Locate every Plasmodium falciparum-infected red blood cell.
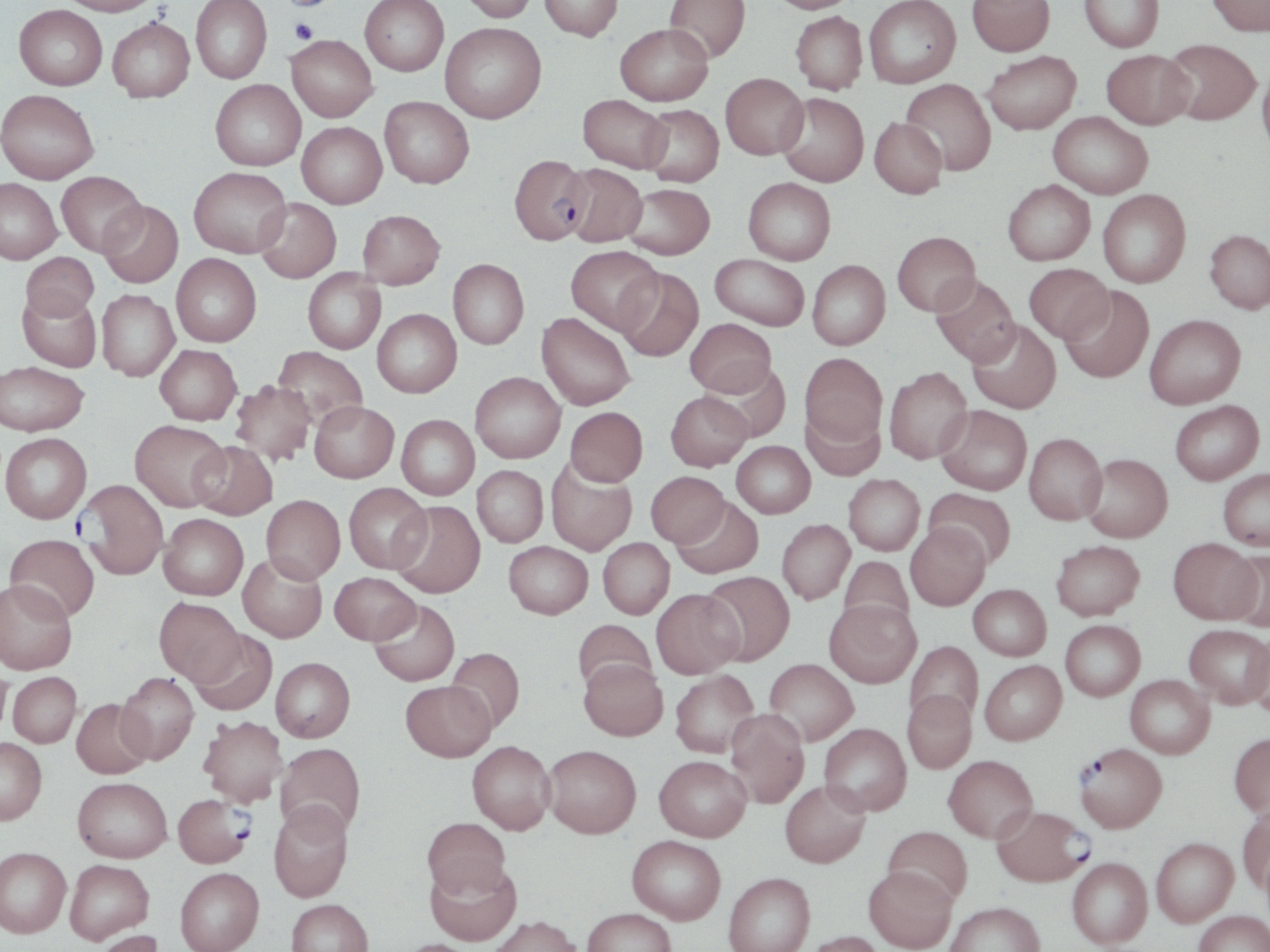

Approximate bounding boxes as (x1,y1)-(x2,y2) corner pairs in pixels.
Plasmodium falciparum-infected red blood cells: (509,154)-(591,244), (77,479)-(168,580), (1075,743)-(1168,832), (173,793)-(253,867), (992,805)-(1091,887).

slide-level diagnosis = Plasmodium falciparum
stain = May-Grünwald-Giemsa
uninfected red blood cell locations = approximate bounding boxes as (x1,y1)-(x2,y2) corner pairs in pixels: (59,0)-(161,16), (191,0)-(272,83), (360,0)-(448,76), (458,0)-(539,22), (540,0)-(623,41), (664,0)-(751,62), (767,0)-(863,13), (863,0)-(961,88), (967,0)-(1054,55), (1079,0)-(1164,52), (1207,0)-(1270,36), (14,4)-(107,90), (790,11)-(868,94), (108,18)-(194,102), (440,22)-(546,123), (615,23)-(712,105), (286,35)-(377,121), (1162,38)-(1261,125), (1101,49)-(1194,129), (982,50)-(1081,134), (1257,64)-(1270,161), (720,73)-(808,159), (210,79)-(306,171), (901,79)-(996,175), (0,89)-(99,183), (777,93)-(869,187), (578,94)-(671,173), (379,96)-(474,188), (639,105)-(724,187), (1048,111)-(1152,199), (869,117)-(947,199), (297,122)-(386,208), (562,163)-(647,247), (189,167)-(291,257), (56,171)-(146,256), (0,177)-(62,264), (743,177)-(835,265), (1003,179)-(1095,265), (622,183)-(715,259), (1097,189)-(1191,287), (254,198)-(341,283), (98,200)-(183,287), (358,209)-(445,288), (1205,229)-(1270,314), (892,231)-(980,316), (566,245)-(662,334), (21,252)-(99,321), (172,253)-(261,347), (710,254)-(809,330), (448,259)-(529,349), (807,260)-(890,350), (1023,263)-(1113,344), (615,267)-(704,362), (303,268)-(385,354), (930,274)-(1020,367), (1060,285)-(1154,383), (17,289)-(102,371), (97,289)-(179,381), (372,309)-(461,397), (536,312)-(636,410), (1144,314)-(1246,408), (685,318)-(776,397), (967,318)-(1061,413), (155,345)-(241,425), (272,345)-(367,429), (800,353)-(887,445), (1,361)-(89,435), (704,361)-(790,442), (884,366)-(972,464), (470,371)-(565,462), (230,380)-(317,466), (666,391)-(753,470), (1170,399)-(1264,485), (309,401)-(399,483), (801,404)-(886,481), (935,405)-(1032,495), (565,407)-(647,487), (397,415)-(479,500), (130,419)-(229,511), (1024,432)-(1107,525), (1,433)-(91,523), (732,440)-(815,518), (190,441)-(277,520), (1081,453)-(1172,542), (545,458)-(637,556), (472,465)-(548,547), (1218,467)-(1270,550), (646,471)-(730,546), (844,474)-(925,555), (343,483)-(431,573), (924,488)-(1016,567), (261,494)-(345,583), (671,497)-(763,579), (390,501)-(485,598), (159,513)-(248,599), (777,519)-(854,604), (905,521)-(990,611), (5,534)-(100,622), (598,537)-(674,619), (1168,538)-(1261,624), (1051,539)-(1145,620), (504,541)-(592,619), (1222,545)-(1270,631), (237,553)-(327,643), (838,556)-(914,632), (701,571)-(795,665), (329,572)-(420,644), (0,579)-(77,675), (968,584)-(1051,660), (651,588)-(744,679), (154,597)-(244,684), (369,599)-(460,686), (825,599)-(921,687), (572,619)-(657,694), (1060,620)-(1145,701), (1184,624)-(1270,708), (188,629)-(277,715), (1247,631)-(1270,712), (905,641)-(983,727), (446,647)-(525,733), (271,657)-(355,742), (579,658)-(667,740), (765,658)-(858,745), (979,660)-(1066,745), (0,661)-(11,743), (670,670)-(759,758), (8,672)-(82,747), (116,673)-(199,764), (1125,675)-(1214,758), (401,680)-(496,761), (903,690)-(976,773), (71,698)-(154,779), (725,709)-(809,808), (198,715)-(288,806), (819,723)-(912,816), (1229,733)-(1270,817), (0,738)-(47,824), (467,740)-(555,834), (275,742)-(366,837), (542,744)-(641,838), (654,755)-(751,841), (943,755)-(1037,842), (73,777)-(172,862), (780,779)-(870,867), (268,801)-(354,902), (1237,806)-(1270,894), (423,817)-(511,899), (882,826)-(973,906), (627,835)-(726,924), (1151,837)-(1238,926), (0,847)-(71,938), (1067,857)-(1152,948), (65,859)-(154,943), (425,859)-(521,945), (864,865)-(958,952), (175,867)-(264,952), (723,872)-(815,952), (286,899)-(373,952), (945,901)-(1044,952), (582,908)-(676,952), (1193,911)-(1270,952), (489,914)-(581,952), (93,929)-(165,952), (804,931)-(886,952), (392,939)-(479,952)
field of view = single
magnification = 1000x
platelet locations = approximate bounding boxes as (x1,y1)-(x2,y2) corner pairs in pixels: (283,0)-(331,11), (288,19)-(320,44)
preparation = thin blood smear
modality = light microscopy
image size = 1270×952 pixels